State which cell type is depicted.
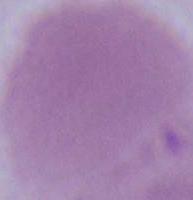
This is an erythrocyte.

Summary:
  - Magnification: 1000x
  - Modality: micrograph